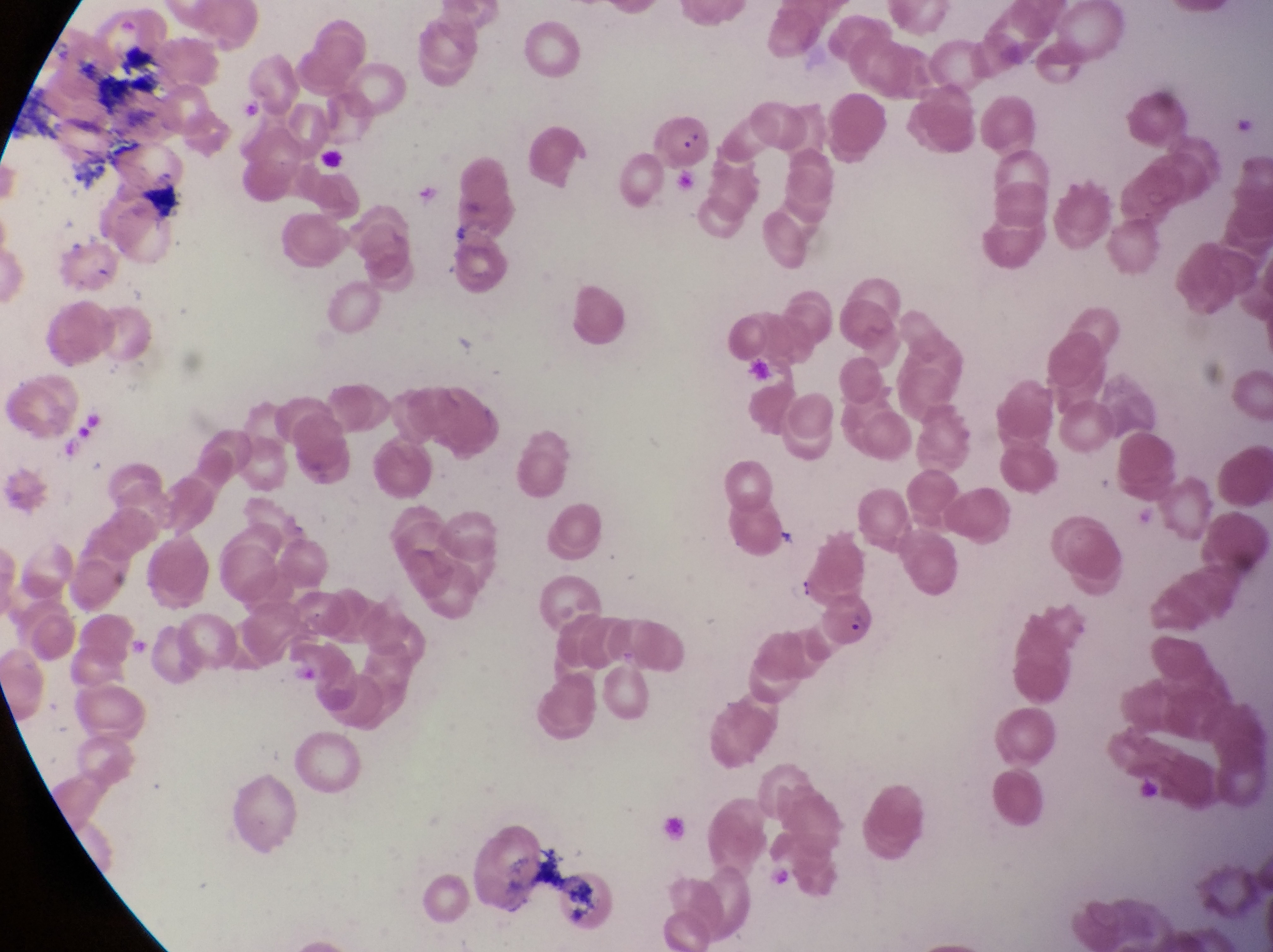
Approximate bounding boxes as (left, top, right, bottom) in pixels.
Summary:
  - Parasitised red blood cell locations: (647, 105, 714, 180), (822, 591, 884, 659)
  - Capture: smartphone photograph through the eyepiece of an Olympus CX-23 microscope
  - Image size: 1273×952 pixels
  - Preparation: thin blood film
  - Magnification: 1000x
  - Field of view: single
  - Country: Uganda